Report the malaria status of this cell.
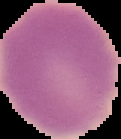
It is uninfected.

{
  "image_type": "cell region segmented out of the field of view; surrounding area masked to black",
  "preparation": "thin blood film",
  "image_size": "121×139 pixels"
}